Comment on the morphology of the erythrocytes.
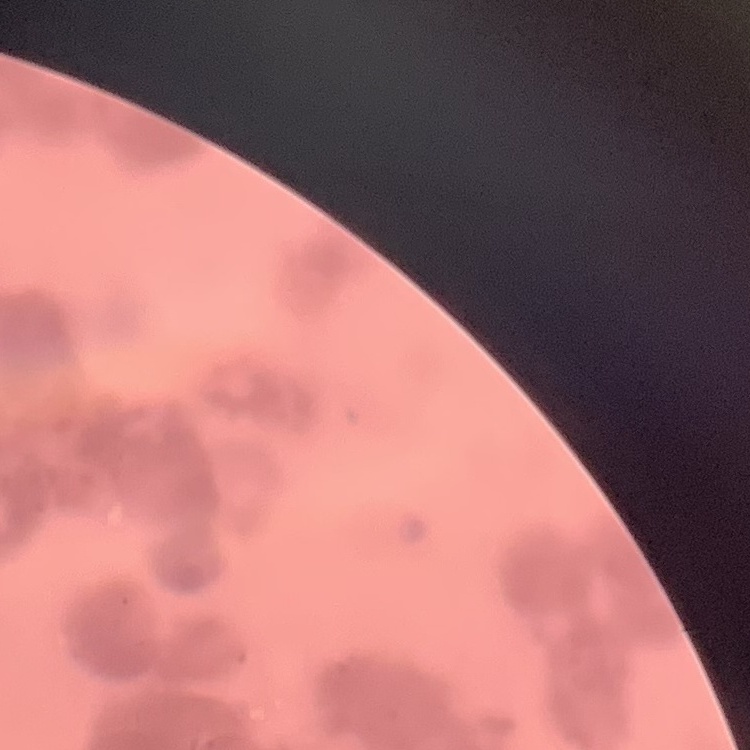

Rouleaux formation.

Summary:
  - Stain: Field's or Giemsa
  - Preparation: thin blood film
  - Image type: square crop of a larger photomicrograph